Name the blood parasite species.
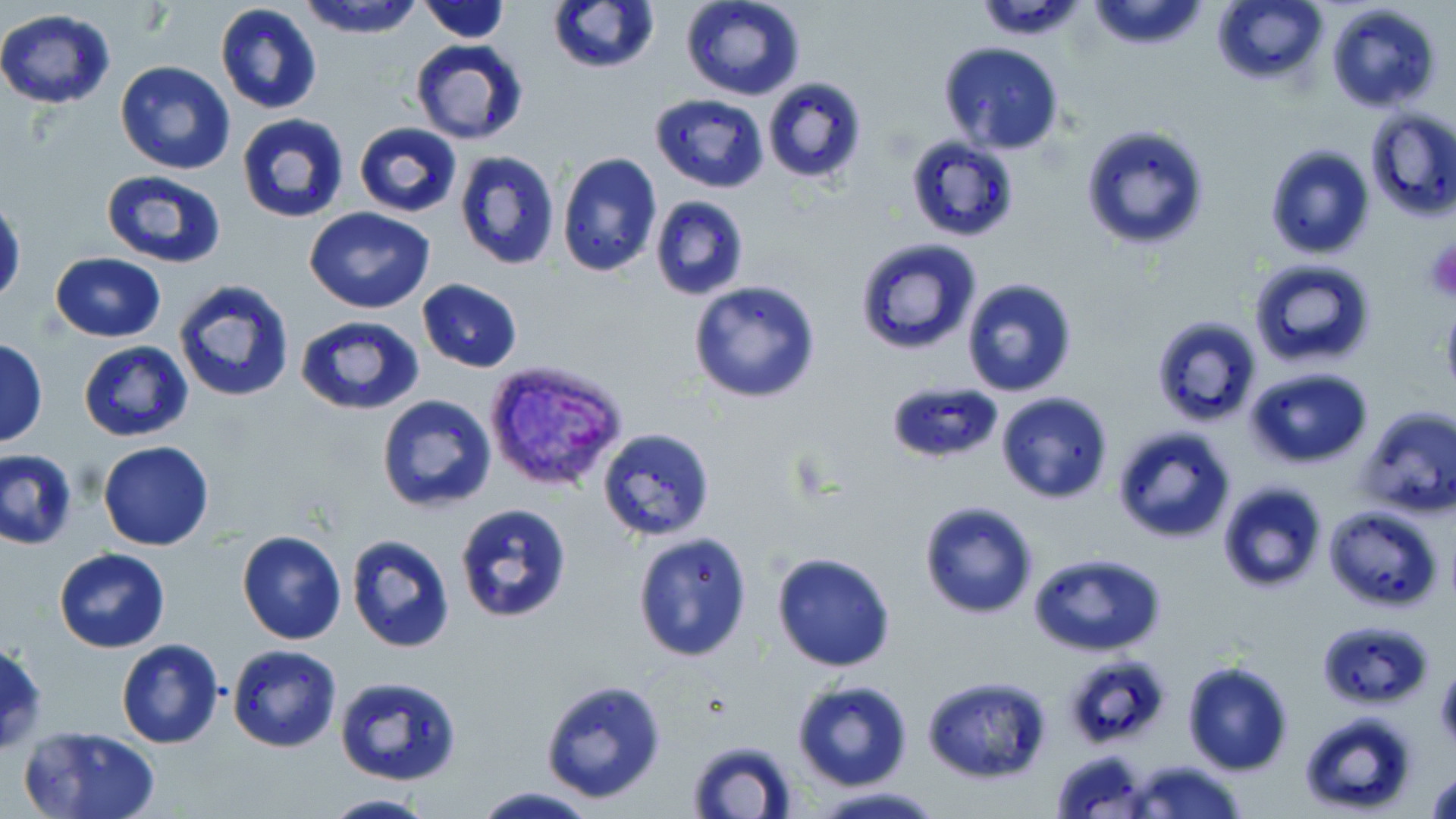
Plasmodium vivax.

Approximate bounding boxes as (x1,y1)-(x2,y2) corner pairs in pixels. Uninfected red blood cell locations: (296,0)-(427,37), (422,0)-(512,43), (548,0)-(659,73), (681,0)-(804,101), (976,0)-(1089,39), (1084,0)-(1210,51), (1211,0)-(1329,89), (214,3)-(323,114), (1326,3)-(1442,114), (0,8)-(116,110), (409,38)-(529,146), (939,41)-(1065,156), (114,61)-(236,176), (762,77)-(867,184), (650,93)-(768,194), (1364,108)-(1456,222), (237,114)-(350,225), (353,123)-(462,217), (1079,124)-(1212,250), (906,136)-(1019,241), (1263,144)-(1377,260), (454,150)-(561,271), (556,152)-(662,277), (99,170)-(226,270), (0,196)-(24,305), (649,196)-(749,301), (305,207)-(435,312), (853,237)-(982,355), (50,252)-(167,341), (1247,257)-(1379,370), (961,277)-(1078,396), (174,278)-(296,402), (416,279)-(523,374), (689,280)-(821,404), (294,314)-(423,416), (1153,314)-(1263,426), (0,340)-(49,446), (79,342)-(193,441), (1245,367)-(1374,469), (885,378)-(1002,464), (995,393)-(1114,505), (375,394)-(498,515), (1356,403)-(1456,521), (1112,425)-(1239,546), (598,429)-(716,543), (98,441)-(214,551), (0,451)-(76,550), (1217,481)-(1326,594), (919,500)-(1038,619), (455,503)-(573,624), (1323,504)-(1444,612), (236,531)-(347,645), (631,531)-(755,664), (347,534)-(455,652), (54,548)-(170,653), (769,552)-(897,674), (1027,552)-(1168,657), (1319,618)-(1434,708), (0,637)-(48,755), (115,639)-(224,749), (227,643)-(341,752), (1180,660)-(1295,776), (334,675)-(462,786), (923,675)-(1051,784), (539,679)-(665,804), (791,679)-(913,791), (1297,711)-(1420,816), (19,726)-(161,819), (686,739)-(800,819), (1049,750)-(1153,818), (1124,760)-(1248,819), (1426,763)-(1456,818), (471,786)-(600,818), (806,786)-(946,818), (322,794)-(438,818). Platelet locations: (1421,237)-(1456,303). Plasmodium vivax-infected red blood cell locations: (482,359)-(631,496). May-Grünwald-Giemsa stain. 1000x magnification. Thin blood smear. Image is 1456×819 pixels. One field of a larger specimen. Light microscopy.